Identify the cell.
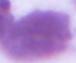

This is an erythrocyte.

modality = photomicrograph
magnification = 1000x